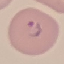

Summary:
  - Result: malaria parasites detected
  - Preparation: thin blood smear
  - Stain: Giemsa
  - Image type: automatically extracted cell patch, resized to 64 × 64 pixels
  - Capture: smartphone through the microscope eyepiece